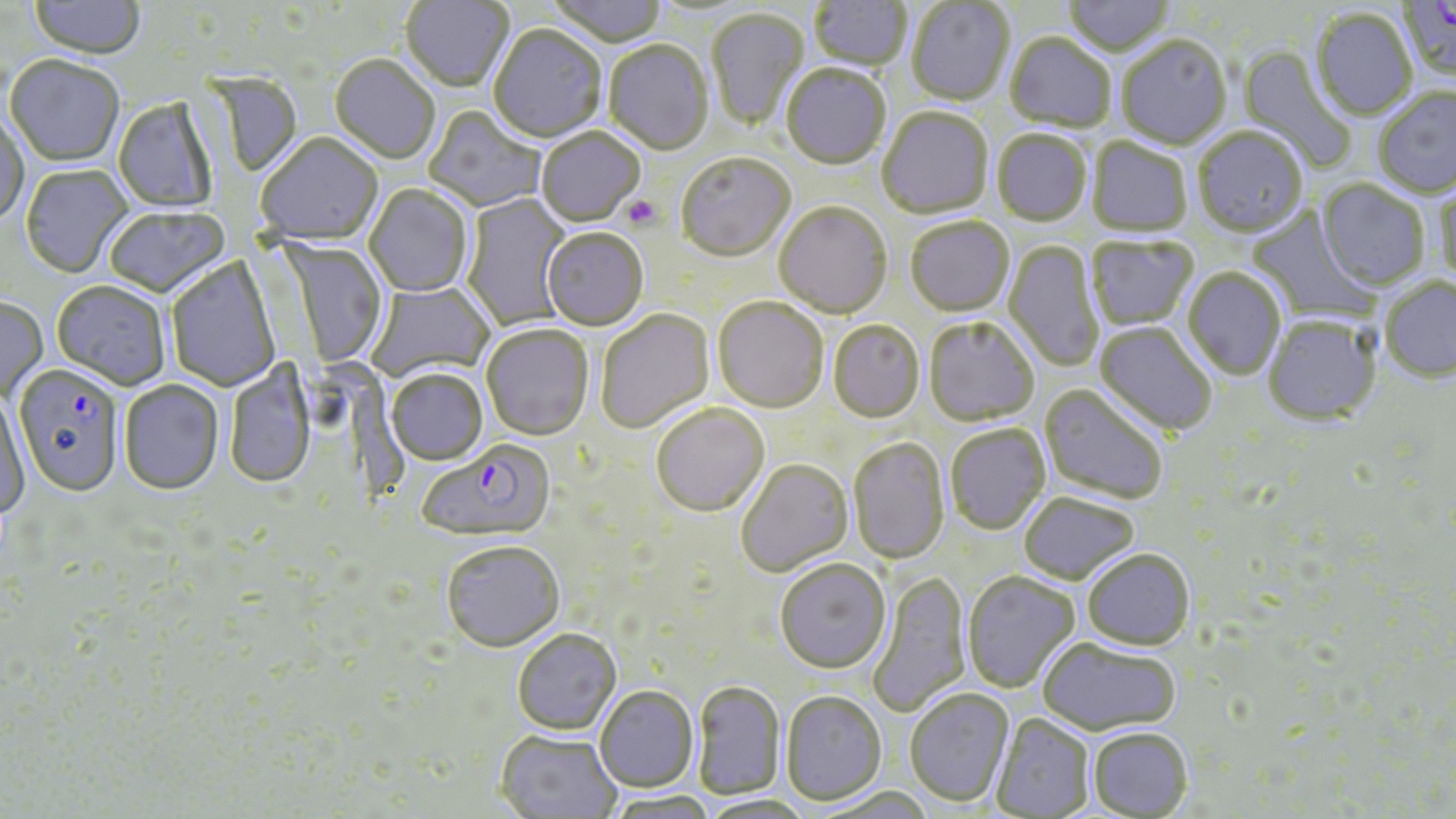

slide-level diagnosis = Plasmodium falciparum
stain = May-Grünwald-Giemsa
preparation = thin blood film
image size = 1456×819 pixels
platelet locations = approximate bounding boxes as (x1, y1, x2, y2) in pixels: (622, 195, 663, 231)
modality = optical microscopy
uninfected red blood cell locations = approximate bounding boxes as (x1, y1, x2, y2) in pixels: (401, 0, 514, 93), (545, 0, 669, 49), (809, 0, 912, 73), (1063, 0, 1176, 59), (29, 1, 146, 61), (907, 1, 1015, 107), (707, 9, 810, 130), (1311, 9, 1418, 122), (488, 27, 607, 145), (1004, 33, 1116, 135), (1116, 37, 1232, 151), (604, 42, 714, 157), (1237, 45, 1357, 173), (329, 56, 440, 166), (5, 57, 125, 167), (781, 66, 891, 172), (1374, 88, 1456, 198), (112, 98, 218, 214), (424, 107, 546, 212), (877, 108, 993, 220), (0, 115, 28, 229), (1193, 128, 1307, 237), (536, 129, 645, 228), (993, 131, 1092, 227), (256, 135, 384, 248), (1087, 138, 1192, 237), (676, 155, 796, 264), (20, 166, 133, 280), (1318, 180, 1429, 291), (1432, 182, 1456, 288), (364, 185, 473, 298), (460, 193, 573, 330), (774, 203, 892, 319), (105, 207, 229, 299), (1247, 207, 1381, 327), (905, 217, 1015, 317), (541, 230, 648, 332), (1085, 236, 1198, 331), (277, 239, 388, 369), (1004, 240, 1104, 372), (167, 257, 280, 392), (1183, 267, 1286, 380), (1379, 277, 1456, 382), (51, 282, 171, 391), (366, 282, 495, 383), (0, 298, 48, 404), (713, 298, 829, 413), (596, 310, 716, 433), (1263, 315, 1381, 425), (923, 316, 1040, 426), (828, 320, 925, 423), (1095, 322, 1218, 437), (482, 325, 594, 442), (225, 359, 316, 491), (386, 370, 487, 466), (119, 381, 225, 496), (1040, 384, 1170, 505), (0, 391, 29, 522), (651, 404, 769, 516), (945, 424, 1050, 535), (848, 437, 949, 564), (735, 458, 852, 576), (1019, 492, 1139, 585), (441, 541, 565, 653), (1082, 548, 1195, 650), (774, 559, 891, 672), (868, 570, 972, 718), (962, 571, 1080, 693), (512, 630, 621, 735), (1038, 638, 1181, 735), (693, 679, 786, 800), (594, 685, 698, 792), (904, 688, 1014, 806), (781, 690, 887, 805), (991, 713, 1094, 818), (1088, 727, 1193, 818), (494, 730, 622, 818), (605, 791, 718, 819), (696, 795, 815, 819)
magnification = 1000x
field of view = one of a larger specimen
Plasmodium falciparum-infected red blood cell locations = approximate bounding boxes as (x1, y1, x2, y2) in pixels: (1397, 0, 1456, 86), (13, 368, 125, 499), (416, 439, 554, 540)